Locate platelets.
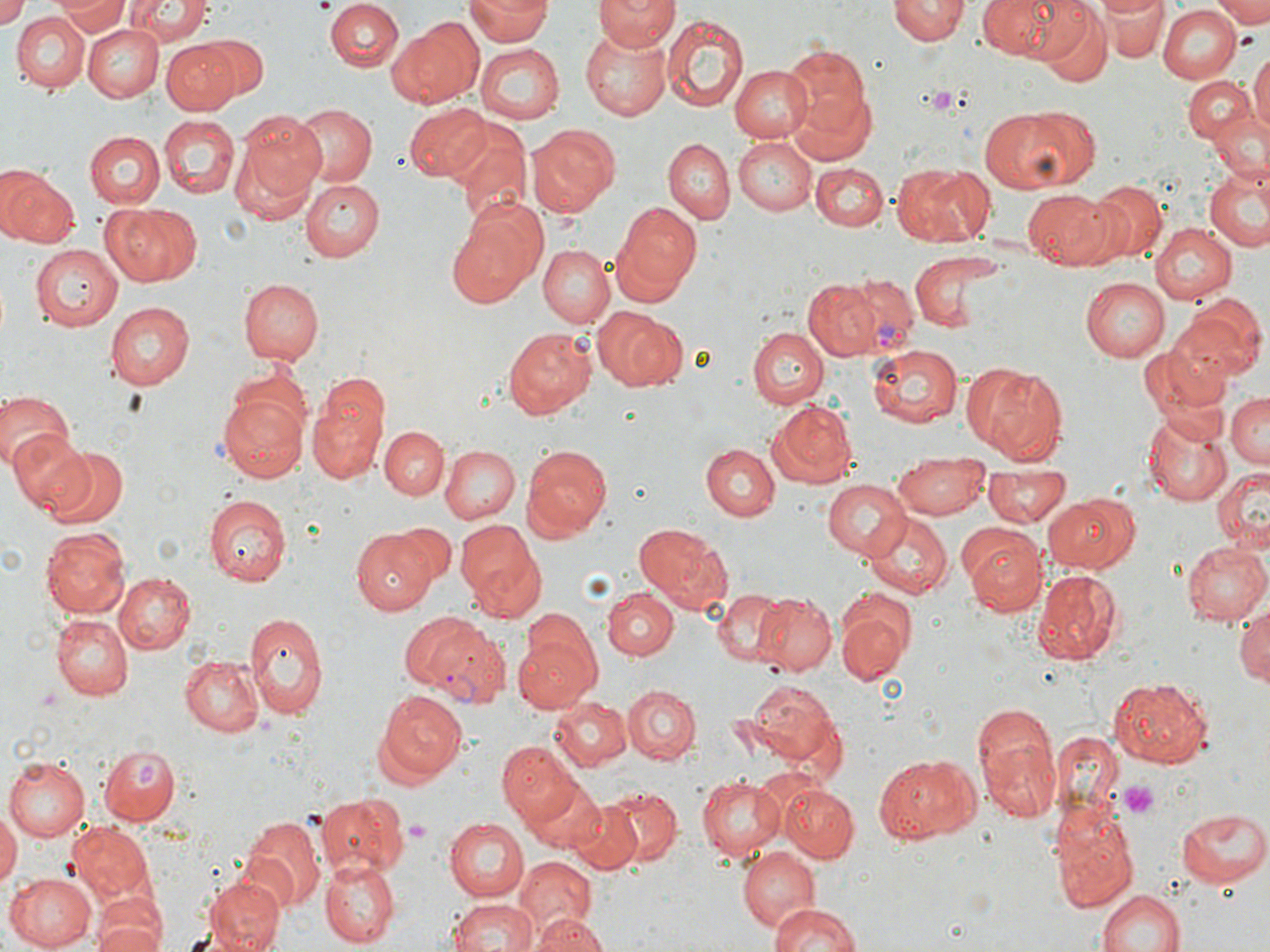

Approximate bounding boxes as named x1/y1/x2/y2 corners in pixels.
Platelets: (x1=312, y1=0, x2=334, y2=11), (x1=930, y1=86, x2=954, y2=114), (x1=1114, y1=779, x2=1163, y2=819), (x1=404, y1=820, x2=427, y2=841).

slide-level diagnosis = Plasmodium vivax
preparation = thin blood film
magnification = 1000x
uninfected red blood cell locations = approximate bounding boxes as named x1/y1/x2/y2 corners in pixels: (x1=53, y1=0, x2=129, y2=38), (x1=120, y1=0, x2=211, y2=44), (x1=467, y1=0, x2=550, y2=44), (x1=595, y1=0, x2=677, y2=52), (x1=977, y1=0, x2=1067, y2=59), (x1=1101, y1=0, x2=1167, y2=60), (x1=1214, y1=0, x2=1270, y2=25), (x1=0, y1=1, x2=29, y2=29), (x1=326, y1=1, x2=403, y2=71), (x1=888, y1=1, x2=969, y2=46), (x1=1030, y1=3, x2=1111, y2=85), (x1=1157, y1=5, x2=1240, y2=82), (x1=326, y1=7, x2=473, y2=85), (x1=13, y1=12, x2=89, y2=93), (x1=662, y1=16, x2=749, y2=109), (x1=388, y1=19, x2=485, y2=109), (x1=81, y1=23, x2=164, y2=102), (x1=581, y1=30, x2=671, y2=121), (x1=201, y1=35, x2=270, y2=100), (x1=161, y1=39, x2=239, y2=114), (x1=475, y1=44, x2=562, y2=122), (x1=781, y1=45, x2=871, y2=136), (x1=1249, y1=46, x2=1270, y2=145), (x1=729, y1=64, x2=812, y2=142), (x1=1183, y1=75, x2=1255, y2=145), (x1=790, y1=90, x2=875, y2=166), (x1=404, y1=101, x2=488, y2=184), (x1=288, y1=103, x2=376, y2=188), (x1=978, y1=105, x2=1087, y2=191), (x1=232, y1=110, x2=328, y2=210), (x1=1207, y1=111, x2=1270, y2=186), (x1=157, y1=116, x2=239, y2=199), (x1=449, y1=120, x2=532, y2=223), (x1=527, y1=124, x2=618, y2=215), (x1=85, y1=130, x2=163, y2=209), (x1=665, y1=138, x2=734, y2=223), (x1=734, y1=139, x2=815, y2=217), (x1=812, y1=163, x2=889, y2=231), (x1=891, y1=163, x2=993, y2=246), (x1=1204, y1=163, x2=1270, y2=253), (x1=0, y1=164, x2=78, y2=248), (x1=299, y1=176, x2=384, y2=259), (x1=1093, y1=182, x2=1167, y2=260), (x1=1022, y1=188, x2=1116, y2=269), (x1=102, y1=202, x2=201, y2=286), (x1=616, y1=202, x2=702, y2=296), (x1=446, y1=203, x2=547, y2=309), (x1=1150, y1=222, x2=1236, y2=303), (x1=29, y1=245, x2=123, y2=331), (x1=539, y1=245, x2=613, y2=327), (x1=909, y1=250, x2=1004, y2=334), (x1=1081, y1=277, x2=1169, y2=362), (x1=237, y1=278, x2=323, y2=364), (x1=803, y1=280, x2=882, y2=358), (x1=1169, y1=301, x2=1263, y2=384), (x1=106, y1=302, x2=195, y2=390), (x1=594, y1=306, x2=684, y2=389), (x1=503, y1=326, x2=594, y2=418), (x1=749, y1=327, x2=826, y2=409), (x1=868, y1=343, x2=964, y2=425), (x1=1139, y1=345, x2=1227, y2=434), (x1=980, y1=365, x2=1067, y2=463), (x1=217, y1=383, x2=311, y2=485), (x1=0, y1=386, x2=73, y2=470), (x1=1226, y1=392, x2=1270, y2=467), (x1=308, y1=395, x2=386, y2=486), (x1=768, y1=400, x2=857, y2=490), (x1=1141, y1=410, x2=1232, y2=507), (x1=381, y1=426, x2=450, y2=501), (x1=12, y1=430, x2=95, y2=515), (x1=702, y1=444, x2=779, y2=521), (x1=439, y1=445, x2=519, y2=524), (x1=521, y1=446, x2=611, y2=539), (x1=44, y1=447, x2=131, y2=530), (x1=895, y1=452, x2=989, y2=519), (x1=985, y1=466, x2=1067, y2=529), (x1=1213, y1=468, x2=1270, y2=554), (x1=822, y1=480, x2=912, y2=559), (x1=1045, y1=491, x2=1142, y2=575), (x1=202, y1=495, x2=288, y2=585), (x1=862, y1=513, x2=953, y2=598), (x1=395, y1=520, x2=455, y2=582), (x1=456, y1=520, x2=543, y2=609), (x1=634, y1=523, x2=732, y2=614), (x1=41, y1=527, x2=130, y2=618), (x1=962, y1=528, x2=1048, y2=614), (x1=351, y1=529, x2=432, y2=614), (x1=1182, y1=540, x2=1268, y2=625), (x1=1031, y1=567, x2=1125, y2=665), (x1=113, y1=572, x2=195, y2=654), (x1=603, y1=588, x2=678, y2=659), (x1=714, y1=589, x2=792, y2=667), (x1=756, y1=593, x2=836, y2=675), (x1=838, y1=598, x2=913, y2=682), (x1=1233, y1=600, x2=1270, y2=690), (x1=243, y1=613, x2=327, y2=720), (x1=51, y1=614, x2=132, y2=700), (x1=511, y1=633, x2=600, y2=709), (x1=178, y1=657, x2=263, y2=736), (x1=1105, y1=674, x2=1216, y2=771), (x1=739, y1=679, x2=843, y2=767), (x1=623, y1=684, x2=699, y2=764), (x1=376, y1=689, x2=467, y2=782), (x1=550, y1=700, x2=632, y2=771), (x1=971, y1=700, x2=1060, y2=825), (x1=500, y1=744, x2=585, y2=828), (x1=98, y1=745, x2=178, y2=826), (x1=875, y1=753, x2=976, y2=841), (x1=5, y1=755, x2=90, y2=841), (x1=698, y1=774, x2=786, y2=860), (x1=523, y1=780, x2=605, y2=855), (x1=778, y1=783, x2=858, y2=863), (x1=604, y1=787, x2=682, y2=865), (x1=318, y1=792, x2=409, y2=878), (x1=567, y1=799, x2=646, y2=873), (x1=1049, y1=801, x2=1138, y2=914), (x1=1176, y1=806, x2=1269, y2=887), (x1=0, y1=810, x2=19, y2=893), (x1=238, y1=815, x2=323, y2=913), (x1=443, y1=817, x2=529, y2=902), (x1=68, y1=822, x2=154, y2=902), (x1=738, y1=847, x2=819, y2=932), (x1=512, y1=856, x2=597, y2=937), (x1=320, y1=857, x2=398, y2=947), (x1=5, y1=871, x2=98, y2=951), (x1=203, y1=875, x2=285, y2=952), (x1=1093, y1=886, x2=1190, y2=952), (x1=446, y1=898, x2=539, y2=952), (x1=766, y1=901, x2=860, y2=952), (x1=92, y1=902, x2=166, y2=952), (x1=527, y1=913, x2=608, y2=952)
modality = optical microscopy
image size = 1270×952 pixels
Plasmodium vivax-infected red blood cell locations = approximate bounding boxes as named x1/y1/x2/y2 corners in pixels: (x1=827, y1=272, x2=919, y2=356), (x1=398, y1=608, x2=512, y2=704)
stain = May-Grünwald-Giemsa
field of view = one of a larger specimen